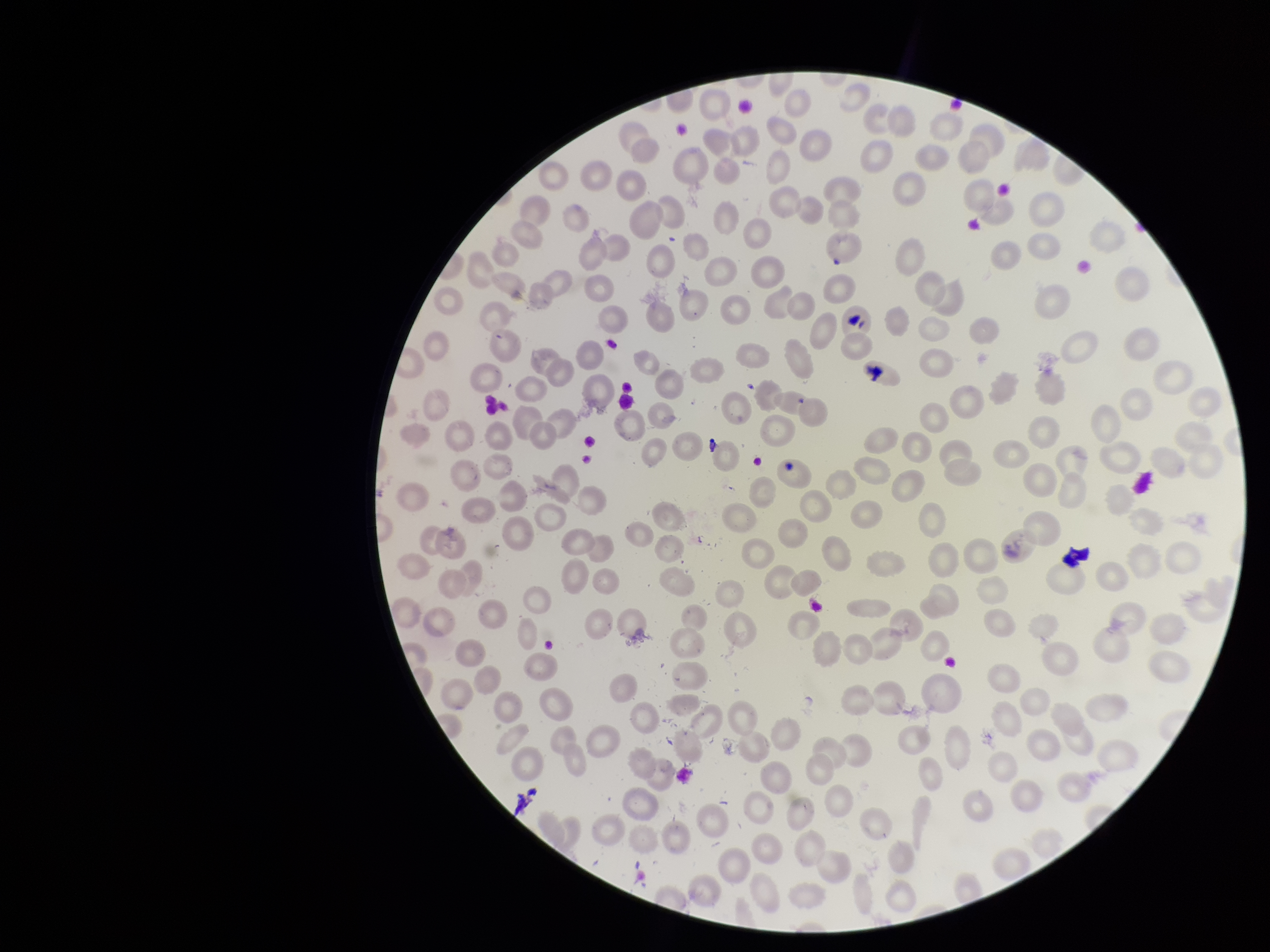 Smartphone photograph taken through the eyepiece of a microscope. Parasitized red blood cells: none seen. Single field of view. Red blood cell count: 196. Preparation: thin. Image is 1270×952 pixels. Species reported for this patient: Plasmodium falciparum. Parasitized red blood cell count: 0. Giemsa stain. Patient malaria status: positive.